State which cell type is depicted.
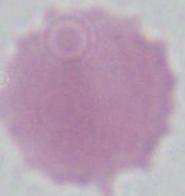

An erythrocyte.

{
  "modality": "micrograph",
  "magnification": "1000x"
}